Assess this cell for malaria.
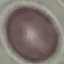
It is uninfected.

Automatically extracted cell patch, resized to 64 × 64 pixels. Thin blood film. Giemsa stain. Photographed with a smartphone camera at the microscope eyepiece.